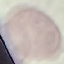

Malaria status: uninfected. Photographed with a smartphone camera at the microscope eyepiece. Automatically extracted cell patch, resized to 64 × 64 pixels. Thin blood smear. Giemsa stain.